Give the position of every malaria parasite.
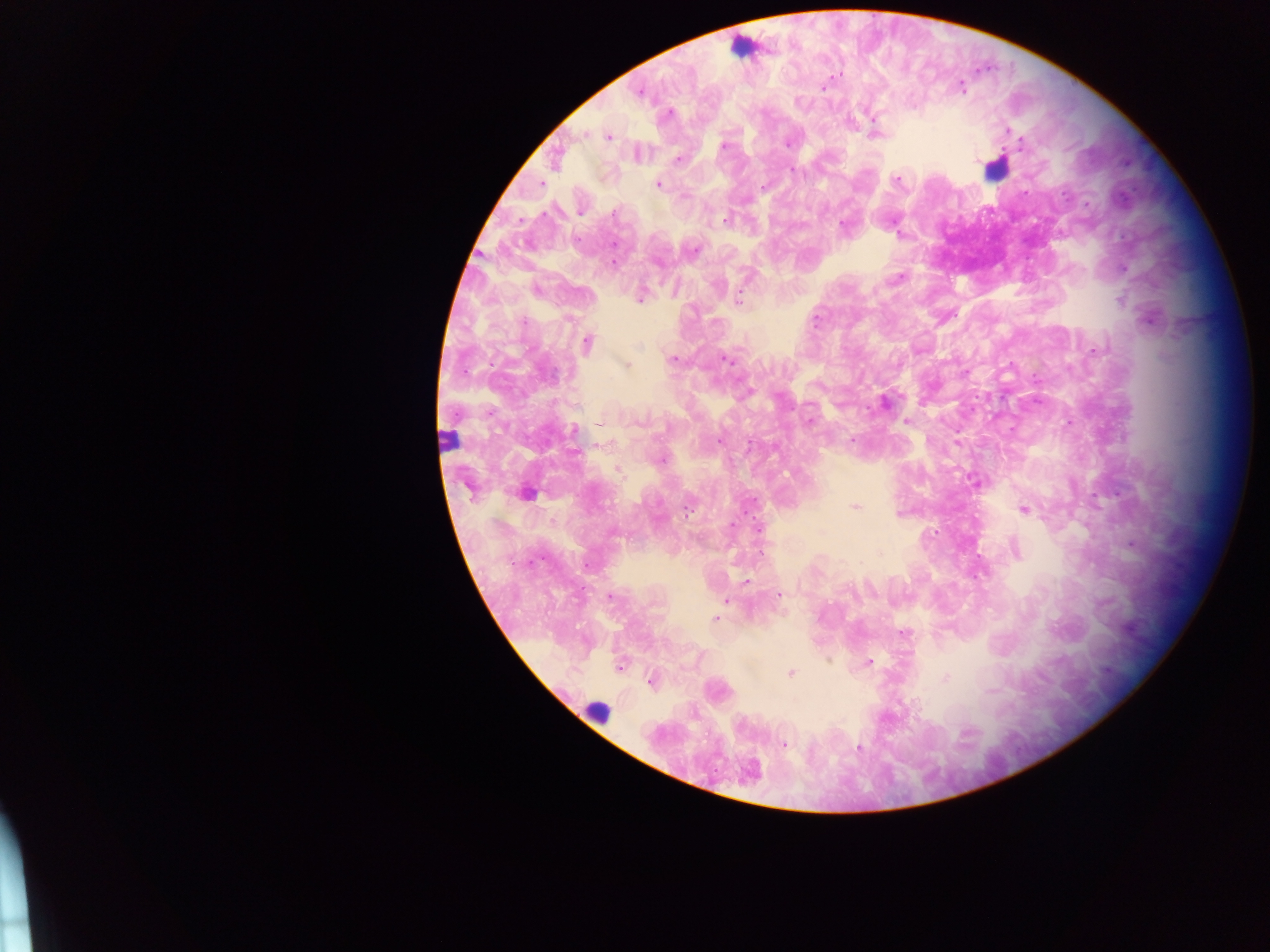

Approximate centers as [x, y] in pixels.
Malaria parasites: [836, 75], [960, 87], [822, 88], [639, 91], [667, 113], [849, 121], [874, 133], [607, 136], [788, 143], [724, 145], [637, 153], [677, 158], [554, 160], [791, 170], [896, 179], [656, 184], [727, 220], [691, 249], [1124, 267], [900, 277], [535, 290], [641, 295], [738, 300], [1149, 317], [586, 344], [1093, 351], [725, 358], [673, 359], [627, 365], [884, 403], [808, 421], [906, 421], [600, 423], [573, 431], [852, 439], [976, 482], [525, 493], [855, 506], [1024, 509], [1131, 545], [1014, 549], [746, 582], [778, 595], [609, 597], [726, 600], [715, 618], [903, 633], [868, 662], [619, 666], [790, 673], [945, 678], [651, 681], [783, 745], [859, 748], [748, 772].

field of view = single
leukocyte locations = approximate centers as [x, y] in pixels: [742, 47], [995, 167], [447, 439], [596, 712]
country = Ghana
image size = 1270×952 pixels
preparation = thick blood smear
capture = mobile-phone photograph through a microscope